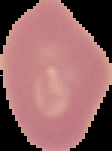 Result: negative for malaria parasites. The area outside the segmented cell region is set to black. From a thin blood film. Image is 112×151 pixels.